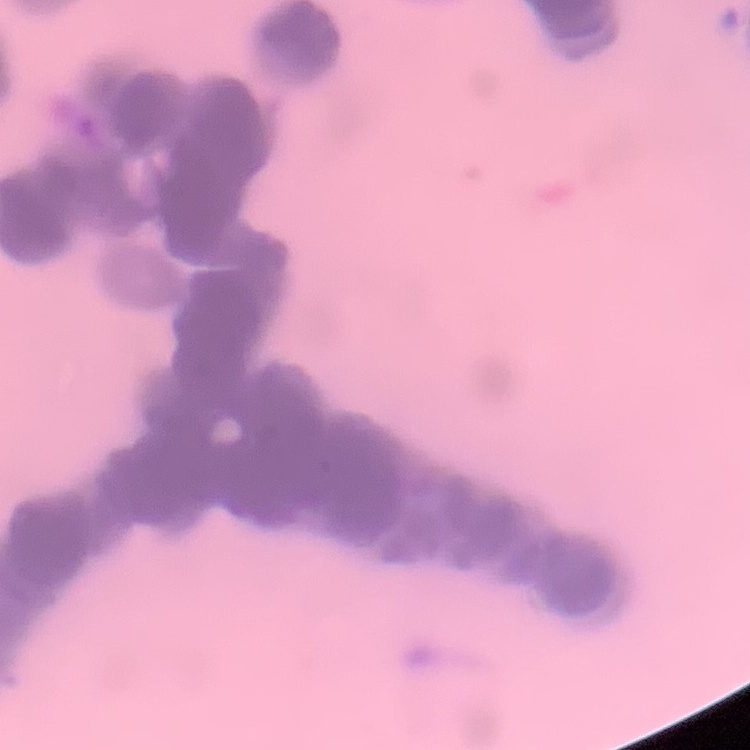

Summary:
  - Red blood cell morphology: rouleaux formation
  - Preparation: thin blood film
  - Stain: Field's or Giemsa
  - Image type: one tile cut from a larger photomicrograph